Locate every leukocyte (white blood cell).
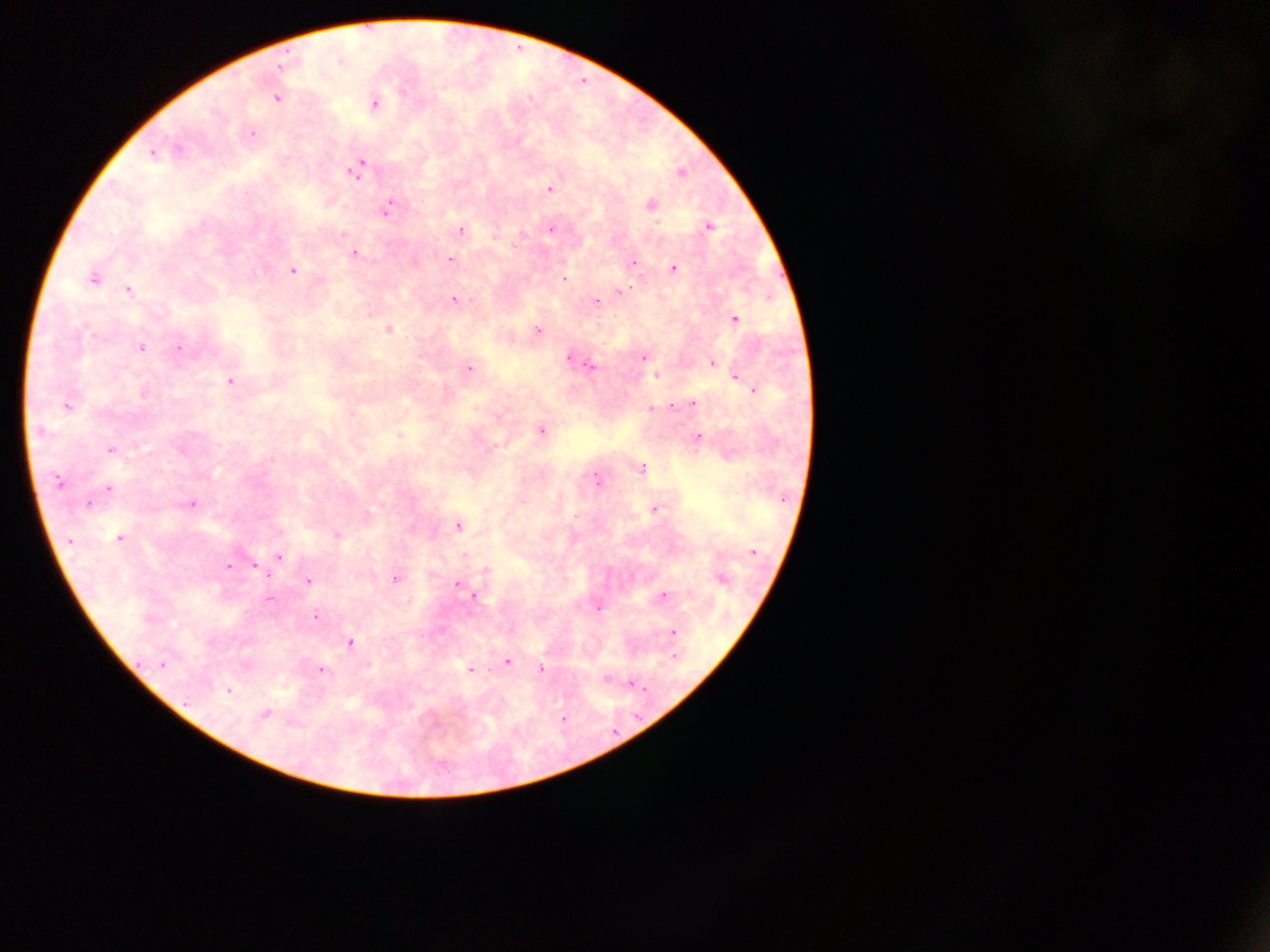
No leukocytes observed.

Approximate centers as x y in pixels. Plasmodium parasite locations: 275 99; 373 103; 251 132; 153 154; 358 168; 678 175; 549 187; 389 207; 550 227; 710 227; 461 230; 495 233; 354 252; 450 259; 413 262; 633 263; 673 267; 293 269; 92 278; 565 279; 130 290; 621 290; 455 299; 596 301; 735 319; 536 329; 140 347; 179 347; 567 357; 644 357; 710 361; 591 366; 469 368; 656 376; 233 377; 735 377; 753 388; 694 401; 67 406; 652 409; 40 431; 542 432; 698 437; 110 449; 642 469; 597 480; 59 483; 110 488; 89 503; 194 503; 656 509; 457 527; 120 536; 69 543; 280 557; 255 566; 226 567; 395 579; 308 581; 457 584; 475 595; 664 595; 270 599; 597 609; 314 616; 673 633; 351 643; 507 661; 161 665; 470 669; 541 669; 321 671; 629 682; 228 692; 264 714; 562 719. Thick blood smear. One field of view. Image is 1270×952 pixels. Collected in Ghana. Photographed through a microscope with a mobile-phone camera.